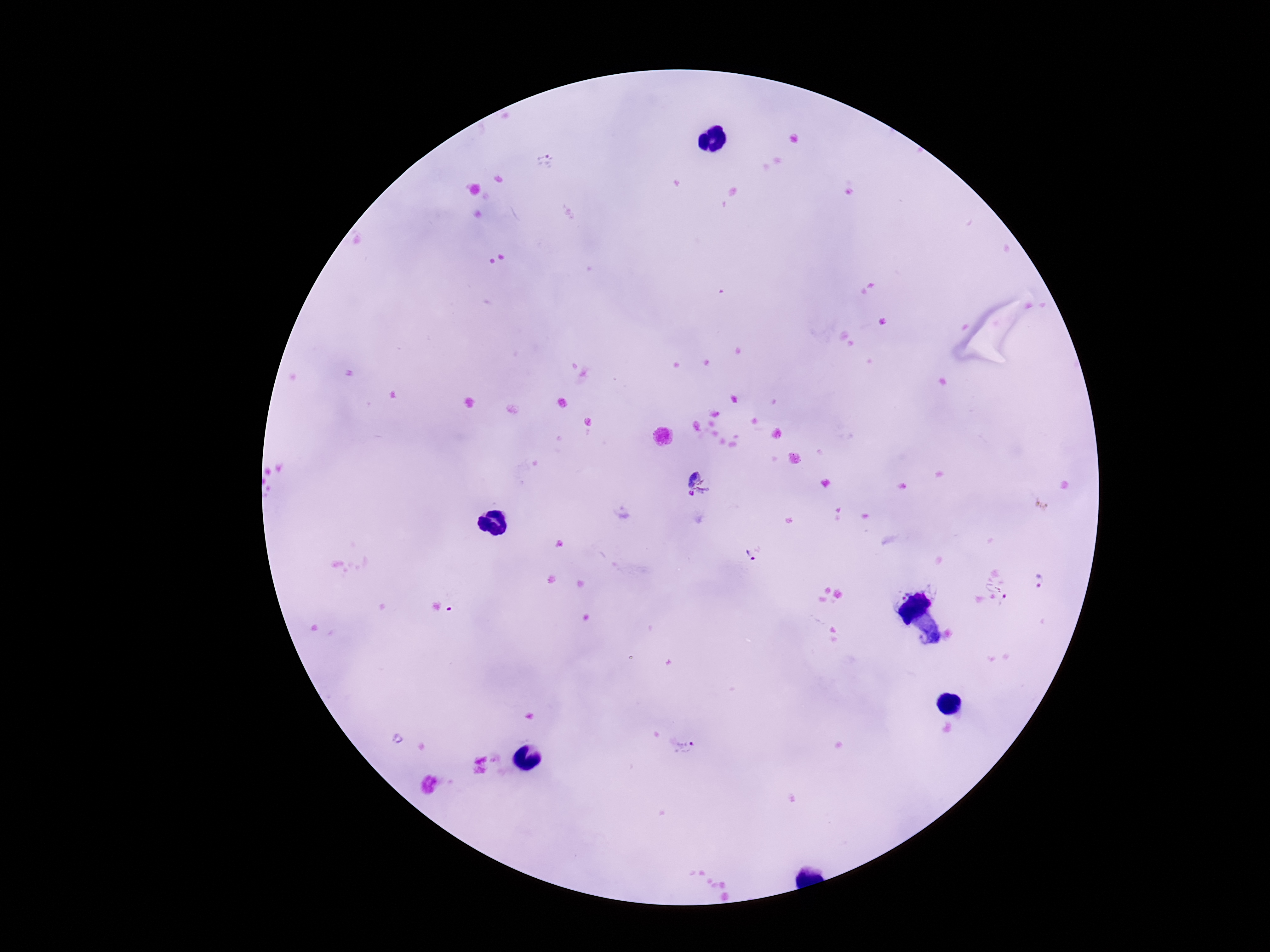

magnification = 100x
stain = Giemsa
field of view = single
preparation = thick peripheral-blood smear
Plasmodium parasite locations = approximate centers as (x, y) in pixels: (545, 161), (697, 485), (753, 553), (1042, 580), (997, 592), (453, 608), (396, 739), (683, 749)
image size = 1270×952 pixels
capture = smartphone camera through the microscope eyepiece
patient malaria status = positive